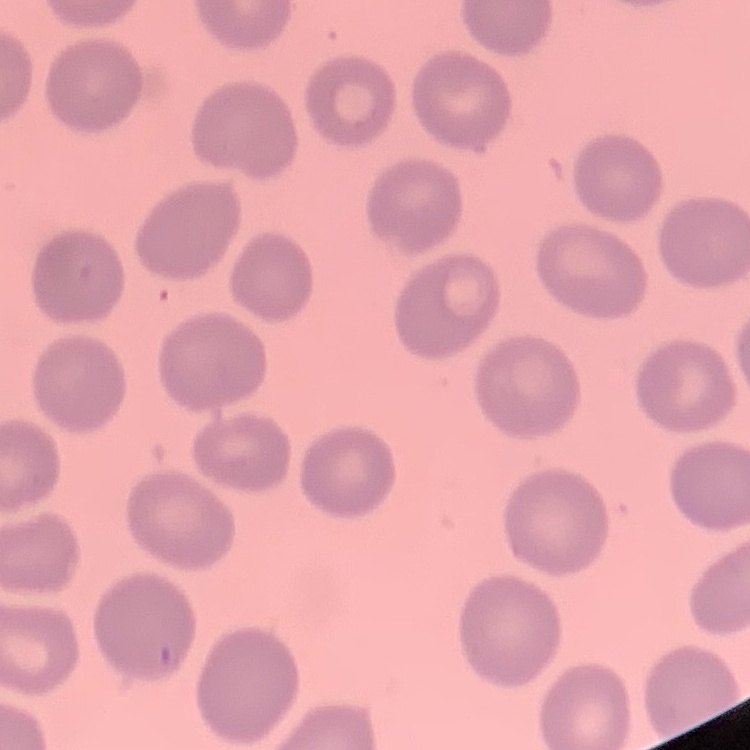

Summary:
  - Erythrocyte morphology: no rouleaux formation
  - Stain: Field's or Giemsa
  - Preparation: thin peripheral smear
  - Image type: square crop of a larger photomicrograph